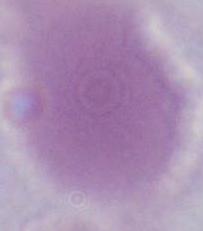

Summary:
  - Modality: micrograph
  - Identification: erythrocyte
  - Magnification: 1000x